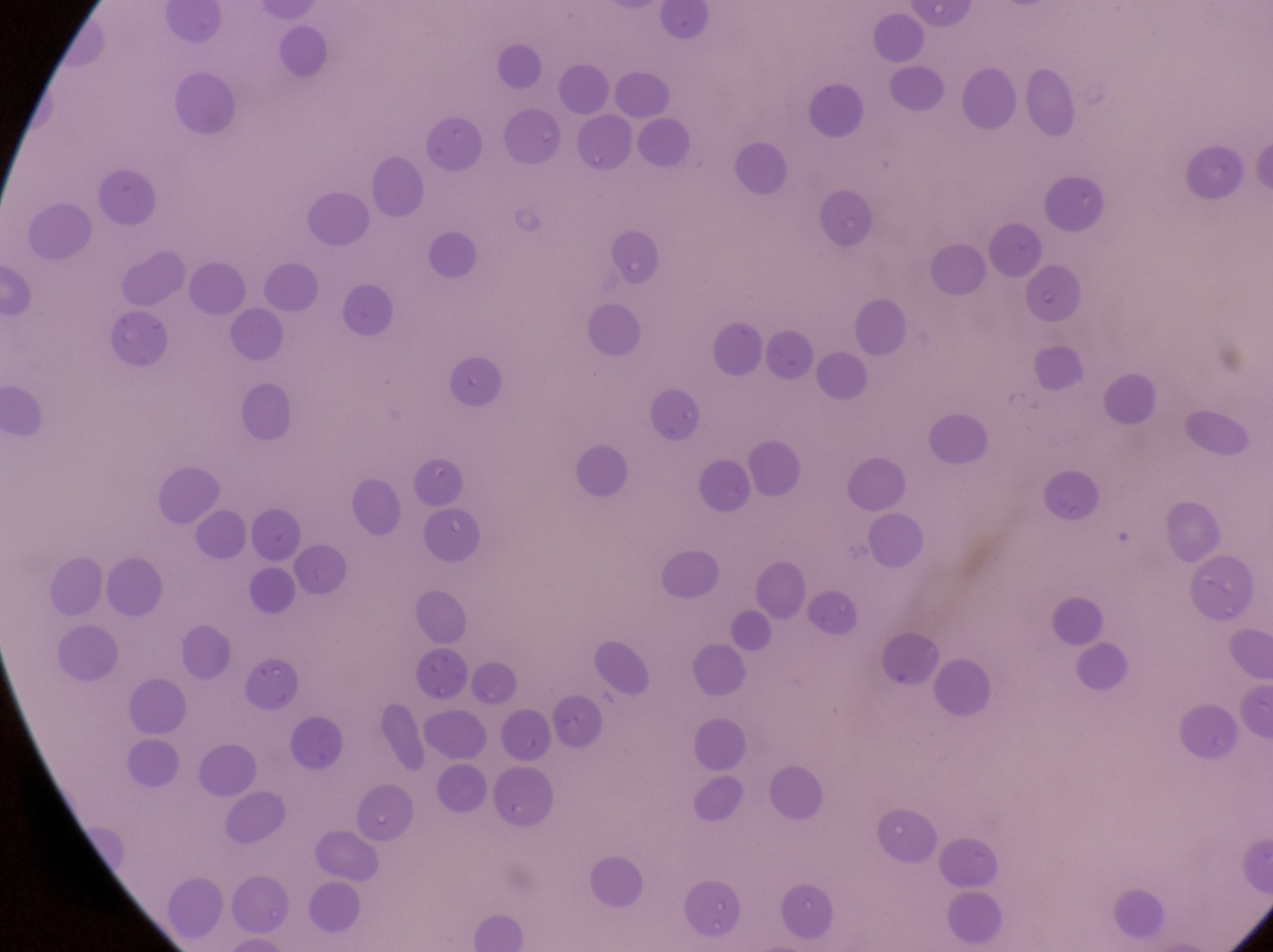
field of view = single
parasitised red blood cell locations = approximate bounding boxes as left top right bottom in pixels: 1029 274 1104 337
image size = 1273×952 pixels
capture = smartphone photograph through the eyepiece of an Olympus CX-23 microscope
country = Uganda
magnification = 1000x
preparation = thin blood smear